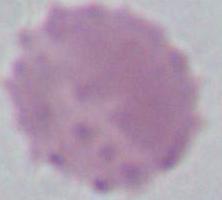 Micrograph. An erythrocyte is seen. Captured at 1000x magnification.